Report the malaria status of this cell.
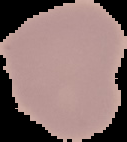

Uninfected.

Summary:
  - Preparation: thin blood film
  - Image size: 127×142 pixels
  - Image type: cell region segmented out of the field of view; surrounding area masked to black